State the blood parasite species.
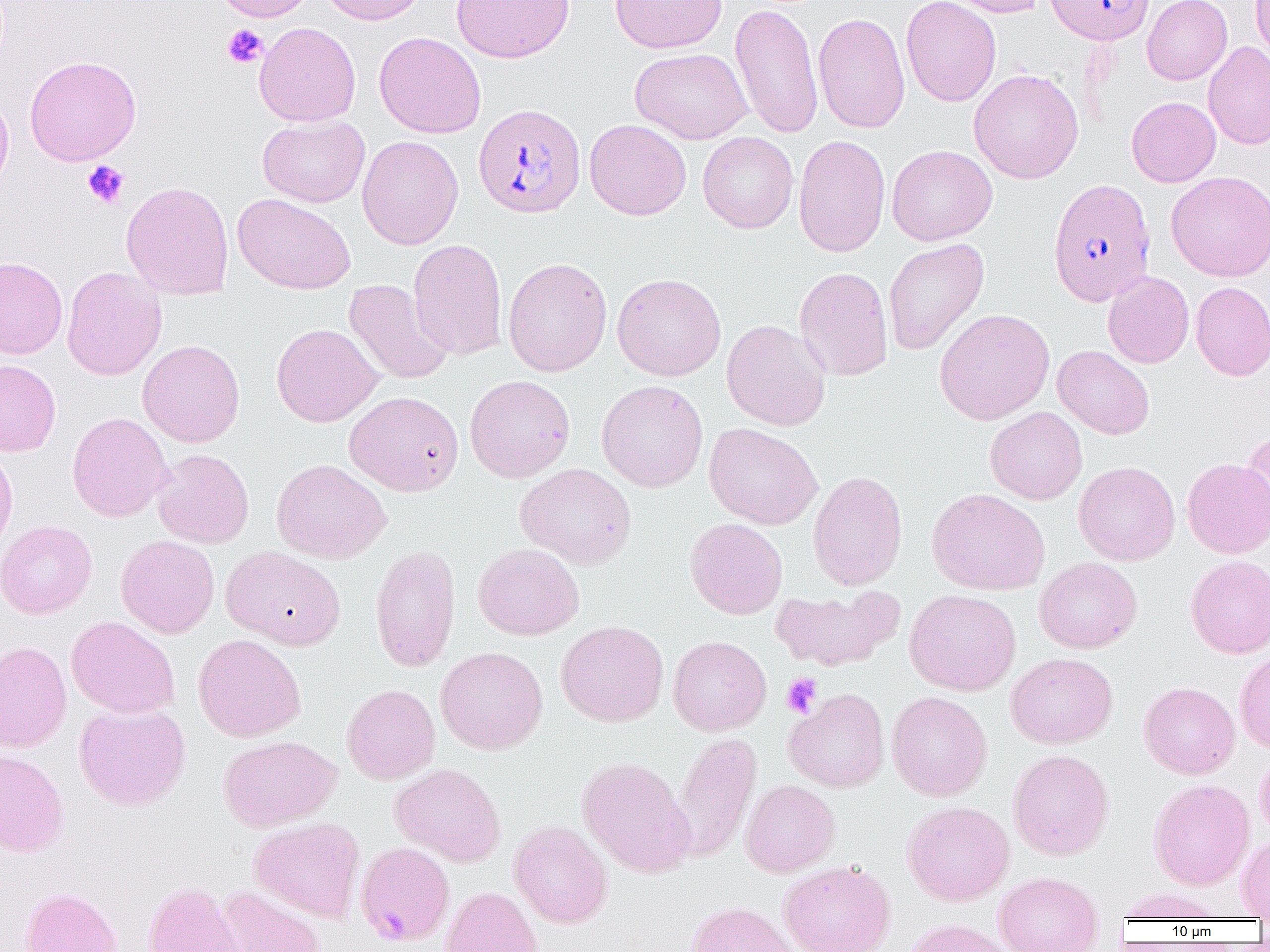

Plasmodium falciparum.

Approximate bounding boxes as named x1/y1/x2/y2 corners in pixels. Plasmodium falciparum-infected red blood cell locations: (x1=1045, y1=0, x2=1154, y2=44), (x1=473, y1=103, x2=586, y2=218), (x1=1047, y1=179, x2=1156, y2=306), (x1=355, y1=841, x2=455, y2=946). Platelet locations: (x1=222, y1=24, x2=268, y2=68), (x1=82, y1=161, x2=130, y2=209), (x1=781, y1=672, x2=822, y2=718). Uninfected red blood cell locations: (x1=212, y1=0, x2=318, y2=22), (x1=319, y1=0, x2=430, y2=25), (x1=451, y1=0, x2=574, y2=63), (x1=610, y1=0, x2=727, y2=54), (x1=900, y1=0, x2=1001, y2=107), (x1=942, y1=0, x2=1049, y2=17), (x1=1142, y1=0, x2=1232, y2=85), (x1=1251, y1=0, x2=1270, y2=66), (x1=730, y1=2, x2=824, y2=139), (x1=813, y1=13, x2=911, y2=133), (x1=254, y1=22, x2=361, y2=127), (x1=374, y1=31, x2=486, y2=138), (x1=1203, y1=42, x2=1270, y2=149), (x1=630, y1=47, x2=753, y2=143), (x1=25, y1=55, x2=141, y2=166), (x1=969, y1=68, x2=1083, y2=183), (x1=0, y1=90, x2=14, y2=198), (x1=1126, y1=96, x2=1221, y2=187), (x1=257, y1=116, x2=370, y2=207), (x1=584, y1=119, x2=692, y2=220), (x1=698, y1=131, x2=799, y2=234), (x1=792, y1=134, x2=891, y2=257), (x1=357, y1=135, x2=463, y2=249), (x1=886, y1=145, x2=997, y2=245), (x1=1165, y1=171, x2=1270, y2=281), (x1=121, y1=181, x2=234, y2=300), (x1=233, y1=193, x2=356, y2=295), (x1=883, y1=238, x2=989, y2=356), (x1=408, y1=239, x2=508, y2=360), (x1=0, y1=257, x2=68, y2=358), (x1=502, y1=257, x2=613, y2=376), (x1=61, y1=266, x2=166, y2=380), (x1=794, y1=266, x2=893, y2=381), (x1=1103, y1=271, x2=1194, y2=368), (x1=612, y1=273, x2=726, y2=381), (x1=343, y1=279, x2=454, y2=385), (x1=1191, y1=281, x2=1270, y2=380), (x1=934, y1=308, x2=1055, y2=425), (x1=721, y1=319, x2=831, y2=431), (x1=272, y1=323, x2=384, y2=427), (x1=137, y1=340, x2=245, y2=447), (x1=1053, y1=345, x2=1155, y2=440), (x1=0, y1=360, x2=61, y2=457), (x1=464, y1=374, x2=576, y2=483), (x1=597, y1=379, x2=708, y2=492), (x1=344, y1=391, x2=464, y2=496), (x1=985, y1=406, x2=1087, y2=505), (x1=67, y1=412, x2=172, y2=522), (x1=704, y1=423, x2=823, y2=529), (x1=1240, y1=429, x2=1270, y2=537), (x1=0, y1=444, x2=18, y2=560), (x1=152, y1=448, x2=254, y2=548), (x1=1182, y1=456, x2=1270, y2=558), (x1=271, y1=458, x2=391, y2=564), (x1=1073, y1=461, x2=1179, y2=566), (x1=515, y1=463, x2=637, y2=569), (x1=807, y1=470, x2=908, y2=590), (x1=927, y1=488, x2=1050, y2=595), (x1=685, y1=518, x2=788, y2=620), (x1=0, y1=520, x2=97, y2=619), (x1=116, y1=535, x2=219, y2=638), (x1=473, y1=543, x2=584, y2=640), (x1=370, y1=544, x2=460, y2=672), (x1=221, y1=546, x2=346, y2=649), (x1=1185, y1=555, x2=1270, y2=658), (x1=1034, y1=557, x2=1142, y2=653), (x1=770, y1=586, x2=902, y2=671), (x1=904, y1=589, x2=1021, y2=696), (x1=66, y1=616, x2=180, y2=719), (x1=555, y1=620, x2=669, y2=727), (x1=193, y1=634, x2=306, y2=742), (x1=668, y1=635, x2=771, y2=736), (x1=0, y1=641, x2=72, y2=753), (x1=436, y1=646, x2=548, y2=754), (x1=1234, y1=649, x2=1270, y2=754), (x1=1005, y1=653, x2=1118, y2=749), (x1=1139, y1=681, x2=1240, y2=779), (x1=341, y1=684, x2=440, y2=784), (x1=784, y1=688, x2=890, y2=792), (x1=886, y1=691, x2=992, y2=801), (x1=74, y1=702, x2=190, y2=811), (x1=670, y1=732, x2=761, y2=862), (x1=218, y1=735, x2=341, y2=832), (x1=0, y1=749, x2=69, y2=857), (x1=1008, y1=749, x2=1114, y2=861), (x1=1255, y1=750, x2=1270, y2=846), (x1=577, y1=756, x2=694, y2=878), (x1=390, y1=763, x2=505, y2=867), (x1=1148, y1=778, x2=1255, y2=890), (x1=740, y1=780, x2=840, y2=877), (x1=901, y1=801, x2=1015, y2=906), (x1=248, y1=816, x2=365, y2=922), (x1=509, y1=820, x2=613, y2=928), (x1=1236, y1=834, x2=1270, y2=919), (x1=778, y1=860, x2=896, y2=952), (x1=993, y1=872, x2=1104, y2=952), (x1=143, y1=882, x2=245, y2=952), (x1=215, y1=886, x2=327, y2=952), (x1=441, y1=886, x2=543, y2=952), (x1=21, y1=887, x2=123, y2=952), (x1=1118, y1=888, x2=1226, y2=922), (x1=686, y1=901, x2=799, y2=952), (x1=901, y1=919, x2=1020, y2=952). One field of a larger specimen. Thin blood smear. Image is 1270×952 pixels. Light microscopy. Captured at 1000x magnification.